Locate every blood parasite and identify its species.
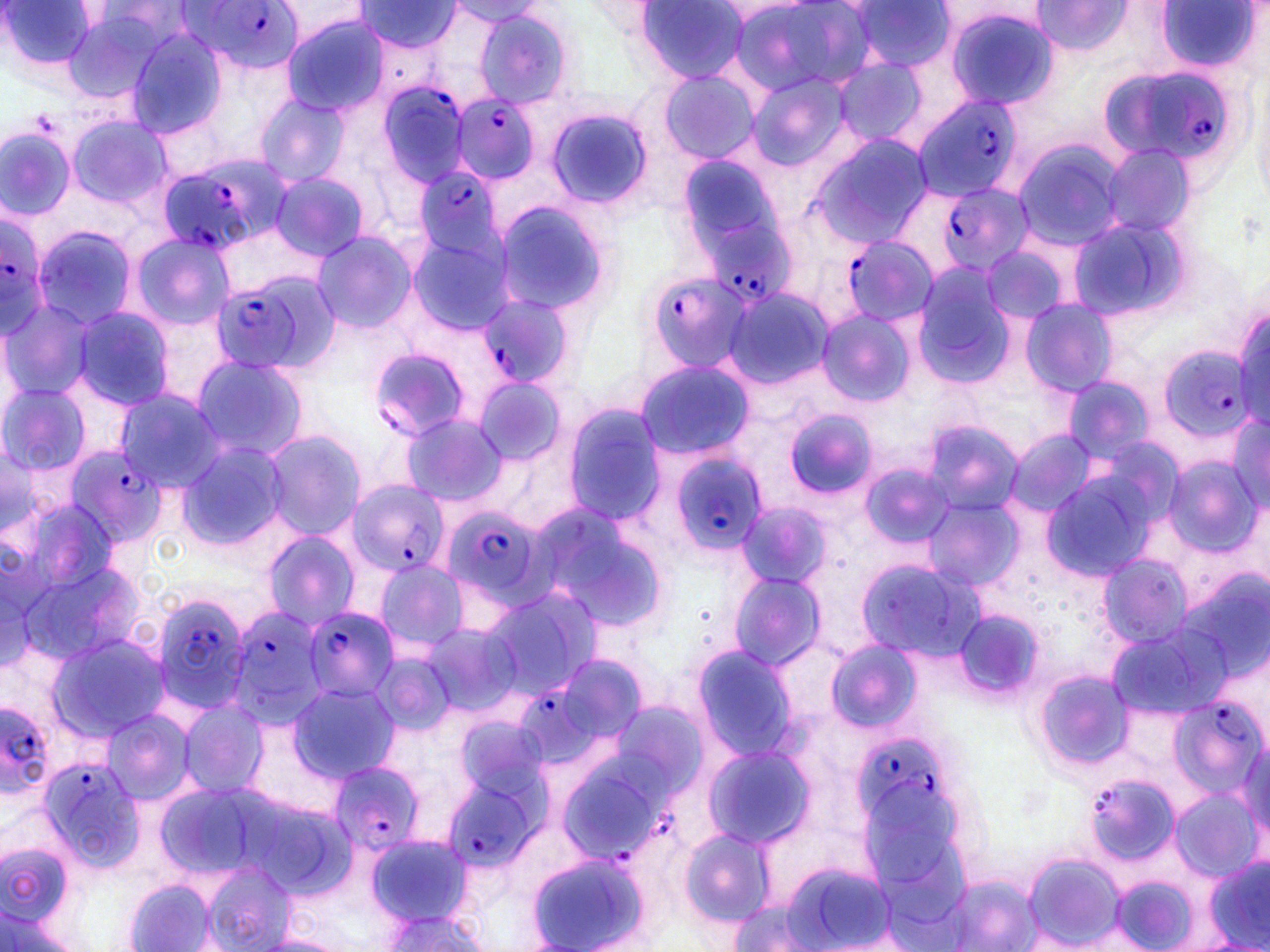
Approximate bounding boxes as [x1, y1, x2, y2] in pixels.
Plasmodium falciparum-infected red blood cells (subset): [183, 1, 300, 74], [1101, 60, 1240, 173], [376, 81, 470, 193], [910, 94, 1022, 202], [454, 95, 541, 183], [159, 151, 288, 258], [411, 162, 505, 265], [936, 181, 1035, 276], [0, 212, 55, 332], [710, 225, 797, 308], [838, 233, 938, 328], [642, 269, 751, 371], [212, 275, 328, 375], [473, 294, 574, 391], [370, 347, 470, 442], [1162, 347, 1260, 439], [63, 444, 166, 550], [661, 447, 766, 558], [346, 480, 450, 580], [441, 503, 553, 611], [150, 596, 251, 712], [223, 605, 327, 729], [304, 607, 400, 705], [517, 691, 602, 763], [1172, 693, 1264, 805], [0, 695, 58, 804], [854, 737, 948, 834], [38, 756, 147, 873], [328, 761, 424, 855], [559, 763, 662, 862], [445, 772, 542, 876], [1085, 776, 1173, 867].
No Plasmodium ovale, Plasmodium malariae, Plasmodium vivax, Babesia divergens, or Trypanosoma brucei observed.

slide-level diagnosis = Plasmodium falciparum
stain = May-Grünwald-Giemsa
field of view = single
preparation = thin blood smear
uninfected red blood cell locations (subset) = approximate bounding boxes as [x1, y1, x2, y2] in pixels: [734, 0, 874, 95], [1, 1, 98, 76], [847, 1, 955, 74], [1030, 1, 1136, 55], [1153, 1, 1261, 76], [355, 2, 462, 53], [450, 2, 547, 25], [635, 2, 748, 85], [56, 5, 178, 105], [939, 5, 1059, 109], [473, 8, 575, 109], [282, 15, 387, 115], [122, 26, 232, 139], [834, 58, 929, 147], [655, 70, 761, 165], [748, 73, 852, 169], [255, 93, 349, 187], [546, 107, 652, 211], [67, 114, 172, 210], [0, 127, 75, 218], [809, 133, 932, 247], [1013, 141, 1126, 250], [1101, 144, 1195, 238], [675, 152, 786, 256], [269, 168, 371, 263], [275, 185, 397, 318], [491, 198, 613, 314], [1066, 216, 1193, 321], [31, 224, 136, 330], [309, 230, 417, 334], [130, 232, 233, 330], [406, 236, 511, 335], [978, 241, 1071, 323], [911, 262, 1018, 384], [720, 287, 833, 392], [0, 299, 99, 403], [1020, 299, 1117, 397], [1231, 302, 1270, 427], [70, 306, 178, 411], [818, 310, 915, 404], [188, 352, 307, 461], [633, 357, 754, 459], [1058, 376, 1157, 466], [0, 382, 93, 477], [112, 388, 227, 492], [563, 405, 666, 523], [782, 408, 879, 500], [1224, 410, 1270, 514], [401, 412, 507, 507], [920, 416, 1021, 520], [1006, 428, 1095, 519], [261, 430, 366, 539], [176, 442, 289, 553], [3, 449, 41, 534], [1161, 457, 1262, 559], [1034, 469, 1162, 582], [922, 493, 1023, 597], [734, 500, 836, 590], [526, 503, 671, 635], [261, 530, 360, 630], [1097, 552, 1196, 651], [371, 558, 470, 655], [726, 569, 828, 675], [480, 585, 602, 700], [419, 622, 518, 721], [1106, 624, 1218, 725], [47, 635, 170, 741], [823, 640, 923, 732], [689, 644, 797, 758], [1035, 671, 1134, 768], [287, 683, 399, 783], [177, 697, 269, 800], [103, 709, 195, 803], [704, 744, 813, 850], [1170, 790, 1259, 878], [678, 826, 775, 928], [364, 832, 474, 928], [527, 849, 652, 952], [1024, 853, 1122, 947], [1, 858, 82, 952], [1205, 858, 1269, 952], [203, 862, 296, 952], [780, 862, 900, 952], [1110, 876, 1197, 950], [126, 878, 214, 952], [725, 899, 825, 951], [375, 909, 489, 952]
modality = light microscopy
image size = 1270×952 pixels
magnification = 1000x